Locate and identify every blood parasite.
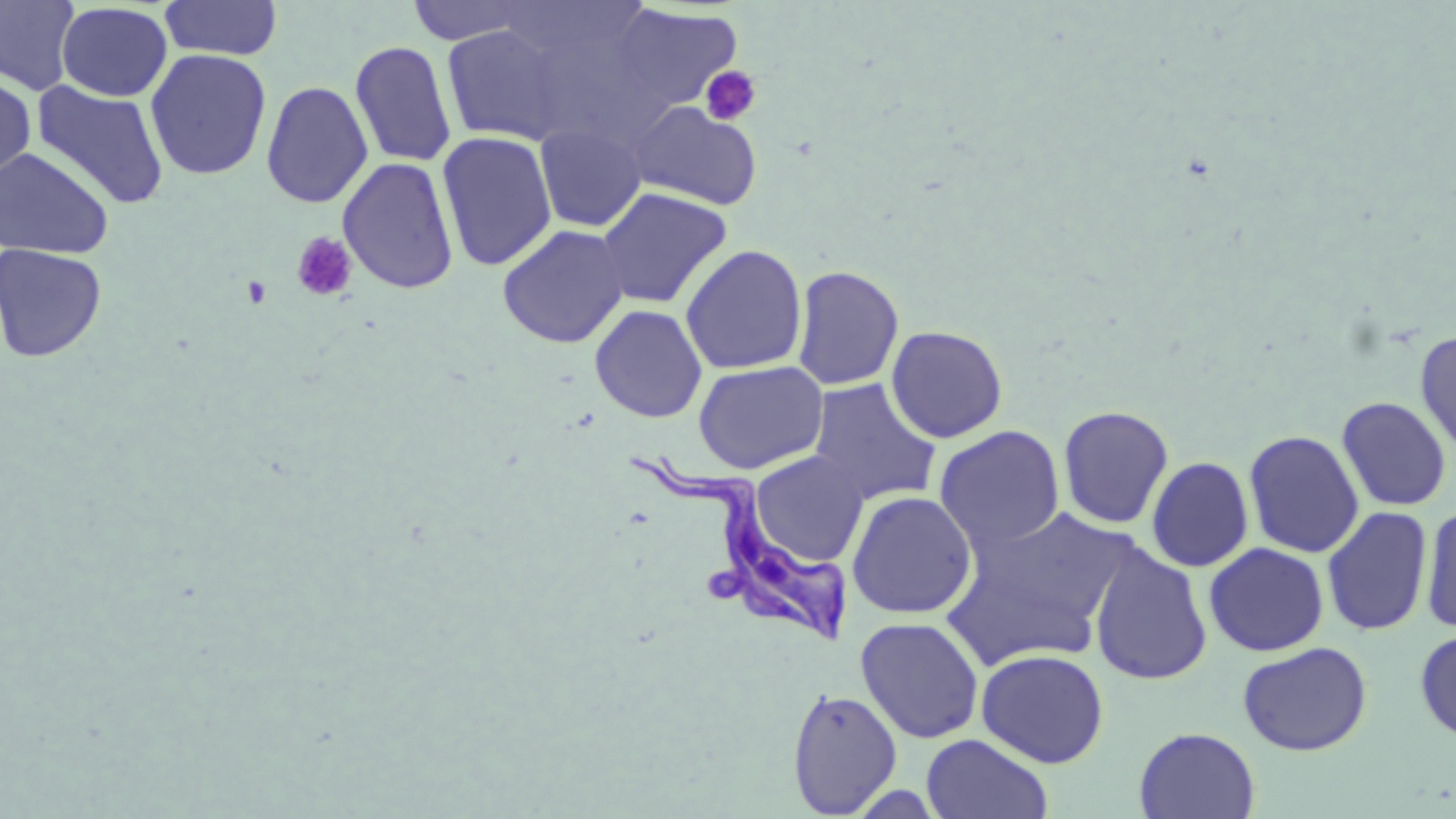
Approximate bounding boxes as named x1/y1/x2/y2 corners in pixels.
Trypanosoma brucei: (x1=636, y1=451, x2=854, y2=652).
No Plasmodium falciparum, Plasmodium ovale, Plasmodium malariae, Plasmodium vivax, or Babesia divergens observed.

{
  "slide_level_diagnosis": "Trypanosoma brucei",
  "modality": "light microscopy",
  "stain": "May-Grünwald-Giemsa",
  "field_of_view": "one of a larger specimen",
  "preparation": "thin blood smear",
  "uninfected_red_blood_cell_locations": "approximate bounding boxes as named x1/y1/x2/y2 corners in pixels: (x1=0, y1=0, x2=81, y2=96), (x1=159, y1=0, x2=284, y2=61), (x1=405, y1=0, x2=536, y2=45), (x1=55, y1=2, x2=173, y2=102), (x1=610, y1=3, x2=743, y2=116), (x1=440, y1=24, x2=570, y2=145), (x1=350, y1=40, x2=457, y2=168), (x1=145, y1=49, x2=271, y2=181), (x1=0, y1=74, x2=36, y2=183), (x1=31, y1=80, x2=170, y2=210), (x1=260, y1=81, x2=373, y2=209), (x1=628, y1=100, x2=763, y2=211), (x1=534, y1=122, x2=647, y2=232), (x1=436, y1=131, x2=558, y2=271), (x1=0, y1=146, x2=115, y2=260), (x1=338, y1=156, x2=459, y2=294), (x1=595, y1=187, x2=732, y2=309), (x1=497, y1=224, x2=630, y2=348), (x1=0, y1=242, x2=107, y2=363), (x1=680, y1=244, x2=807, y2=375), (x1=791, y1=264, x2=904, y2=390), (x1=590, y1=304, x2=707, y2=423), (x1=886, y1=324, x2=1008, y2=443), (x1=1414, y1=329, x2=1456, y2=460), (x1=693, y1=360, x2=828, y2=475), (x1=808, y1=379, x2=942, y2=506), (x1=1336, y1=396, x2=1452, y2=511), (x1=1057, y1=404, x2=1174, y2=529), (x1=934, y1=425, x2=1066, y2=552), (x1=1243, y1=429, x2=1364, y2=558), (x1=751, y1=450, x2=869, y2=565), (x1=1146, y1=455, x2=1254, y2=572), (x1=847, y1=491, x2=977, y2=620), (x1=1419, y1=502, x2=1456, y2=635), (x1=949, y1=504, x2=1136, y2=656), (x1=1322, y1=505, x2=1433, y2=636), (x1=1204, y1=542, x2=1330, y2=657), (x1=1089, y1=544, x2=1212, y2=686), (x1=856, y1=616, x2=984, y2=744), (x1=1414, y1=629, x2=1456, y2=743), (x1=1238, y1=641, x2=1372, y2=756), (x1=976, y1=648, x2=1109, y2=768), (x1=787, y1=688, x2=903, y2=817), (x1=1134, y1=727, x2=1260, y2=818), (x1=921, y1=733, x2=1053, y2=819)",
  "platelet_locations": "approximate bounding boxes as named x1/y1/x2/y2 corners in pixels: (x1=699, y1=65, x2=762, y2=126), (x1=291, y1=231, x2=358, y2=302), (x1=241, y1=276, x2=273, y2=309)",
  "image_size": "1456×819 pixels",
  "magnification": "1000x"
}